Give the extent of all Plasmodium falciparum-infected red blood cells.
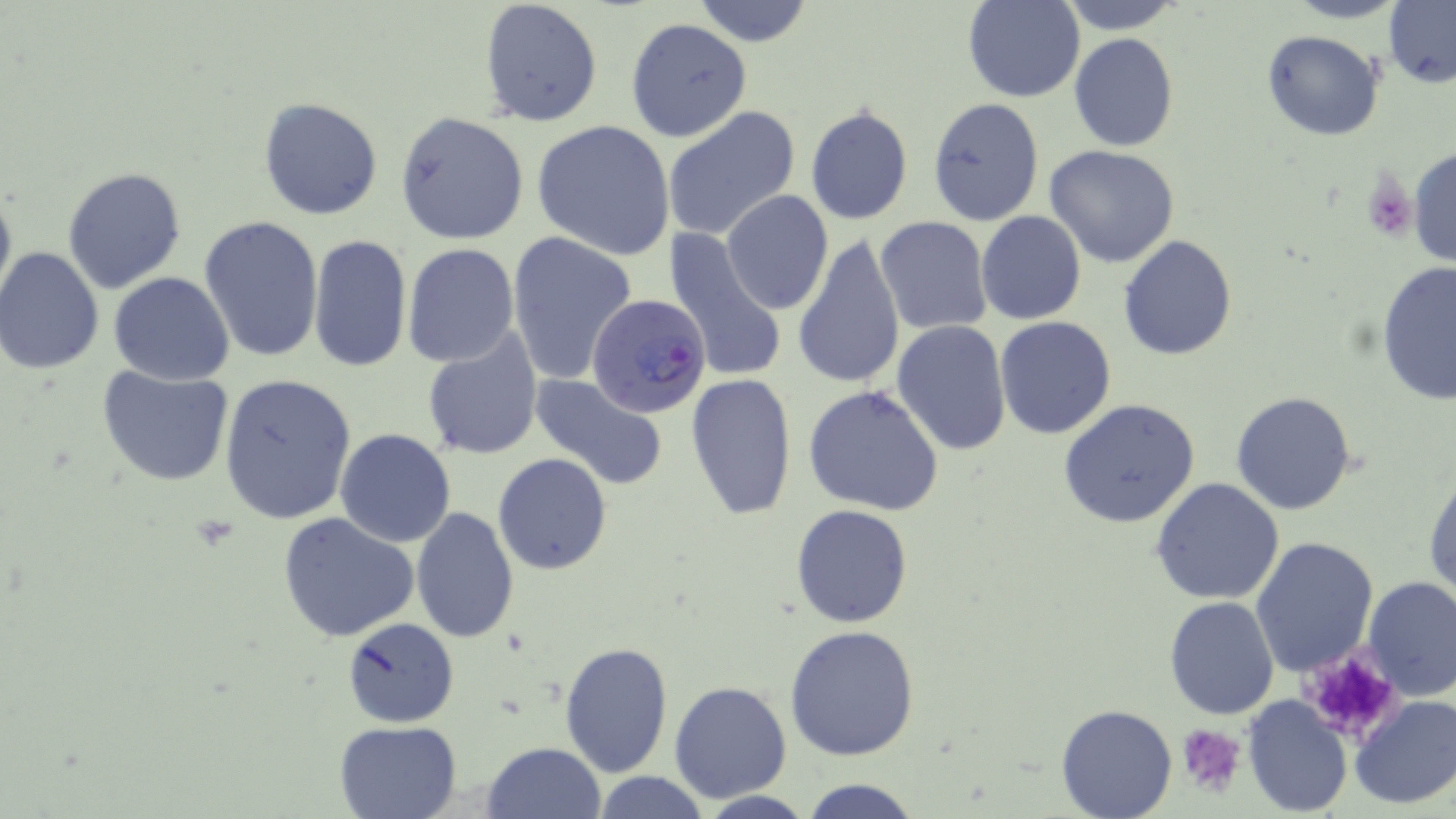
Approximate bounding boxes as [x1, y1, x2, y2] in pixels.
Plasmodium falciparum-infected red blood cells: [586, 293, 712, 422].

Platelet locations: [1362, 173, 1415, 240], [1295, 646, 1403, 743], [1176, 724, 1247, 794]. Uninfected red blood cell locations: [478, 0, 603, 125], [691, 0, 816, 48], [963, 0, 1085, 102], [1057, 0, 1183, 33], [1284, 0, 1410, 24], [1383, 1, 1455, 87], [626, 17, 752, 141], [1262, 31, 1384, 142], [1068, 33, 1179, 152], [258, 97, 383, 221], [927, 98, 1044, 227], [662, 104, 801, 243], [804, 106, 915, 225], [395, 112, 529, 244], [532, 119, 676, 260], [1045, 146, 1180, 267], [1408, 146, 1455, 267], [63, 167, 187, 292], [0, 180, 16, 311], [721, 190, 833, 315], [975, 211, 1087, 326], [198, 214, 325, 363], [875, 217, 992, 334], [505, 230, 639, 384], [663, 231, 787, 384], [794, 233, 906, 389], [307, 234, 411, 375], [1118, 235, 1238, 359], [402, 243, 519, 366], [0, 247, 105, 375], [1376, 262, 1456, 404], [108, 271, 234, 386], [993, 316, 1117, 439], [893, 320, 1012, 455], [422, 335, 543, 460], [98, 364, 234, 487], [530, 372, 668, 489], [218, 373, 358, 524], [684, 374, 797, 523], [802, 383, 949, 517], [1231, 390, 1359, 515], [1057, 398, 1200, 528], [335, 429, 455, 547], [493, 453, 612, 575], [1424, 463, 1456, 603], [1152, 477, 1285, 605], [791, 504, 912, 627], [411, 508, 520, 646], [277, 513, 420, 643], [1250, 535, 1380, 678], [1361, 576, 1455, 700], [1164, 596, 1281, 719], [341, 616, 459, 727], [786, 625, 918, 761], [558, 639, 673, 778], [668, 679, 794, 804], [1348, 694, 1456, 811], [1242, 695, 1352, 815], [1054, 702, 1178, 818], [332, 720, 461, 819], [481, 741, 607, 819], [592, 770, 710, 819], [798, 778, 923, 819]. Slide-level diagnosis: Plasmodium falciparum. Optical microscopy. Single field of view. Image is 1456×819 pixels. May-Grünwald-Giemsa stain. Thin blood film. Captured at 1000x magnification.